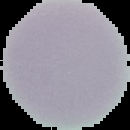 Image is 130×130 pixels. Malaria status: uninfected. Segmented cell region on a black background. From a thin blood film.